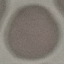

malaria status = uninfected
stain = Giemsa
preparation = thin blood film
image type = automatically extracted cell patch, resized to 64 × 64 pixels
capture = smartphone through the microscope eyepiece